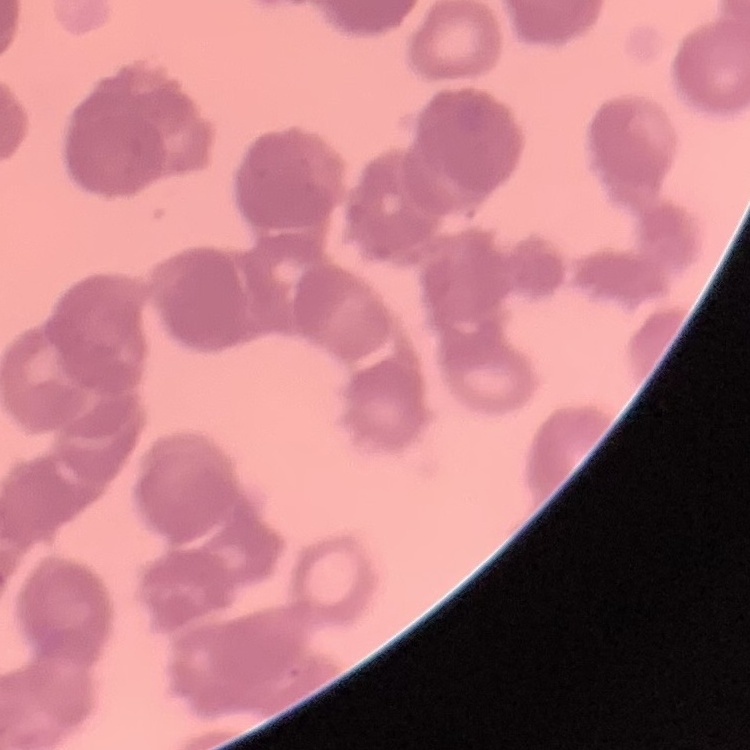
erythrocyte morphology = rouleaux formation
image type = square crop of a larger photomicrograph
stain = Field's or Giemsa
preparation = thin blood film